Give the position of every Plasmodium parasite.
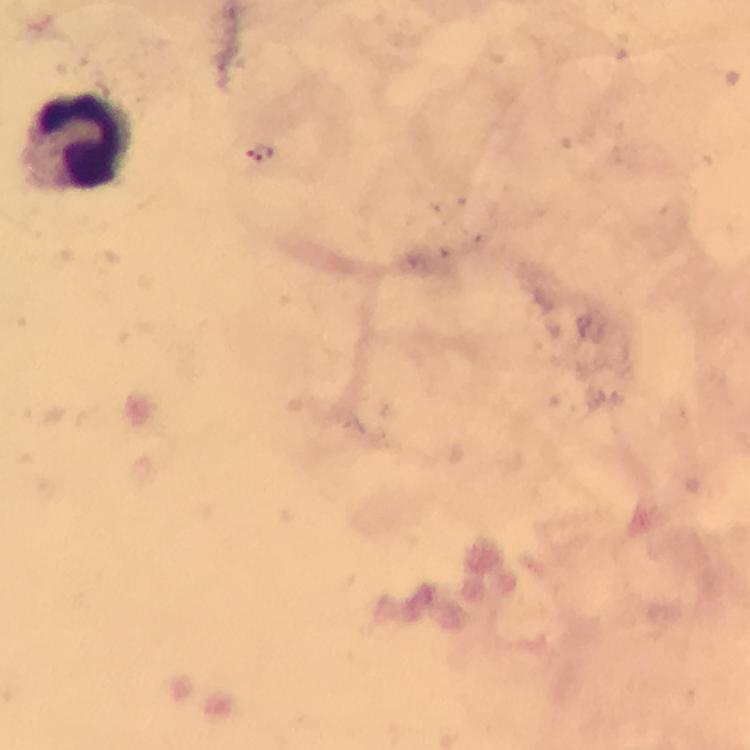
No Plasmodium parasites seen.

{
  "leukocyte_locations": "approximate centers as [x, y] in pixels: [78, 140]",
  "cropped_from": "one field of view",
  "immersion_oil": "used",
  "preparation": "thick smear",
  "image_size": "750×750 pixels",
  "capture": "smartphone photograph through a microscope",
  "magnification": "100x",
  "context": "from a diagnostic examination for malaria",
  "stain": "Giemsa"
}